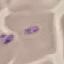

Summary:
  - Malaria status: uninfected
  - Image type: cell patch, automatically extracted from a larger field of view and resized to 64 × 64 pixels
  - Stain: Giemsa
  - Preparation: thin blood film
  - Capture: smartphone through the microscope eyepiece